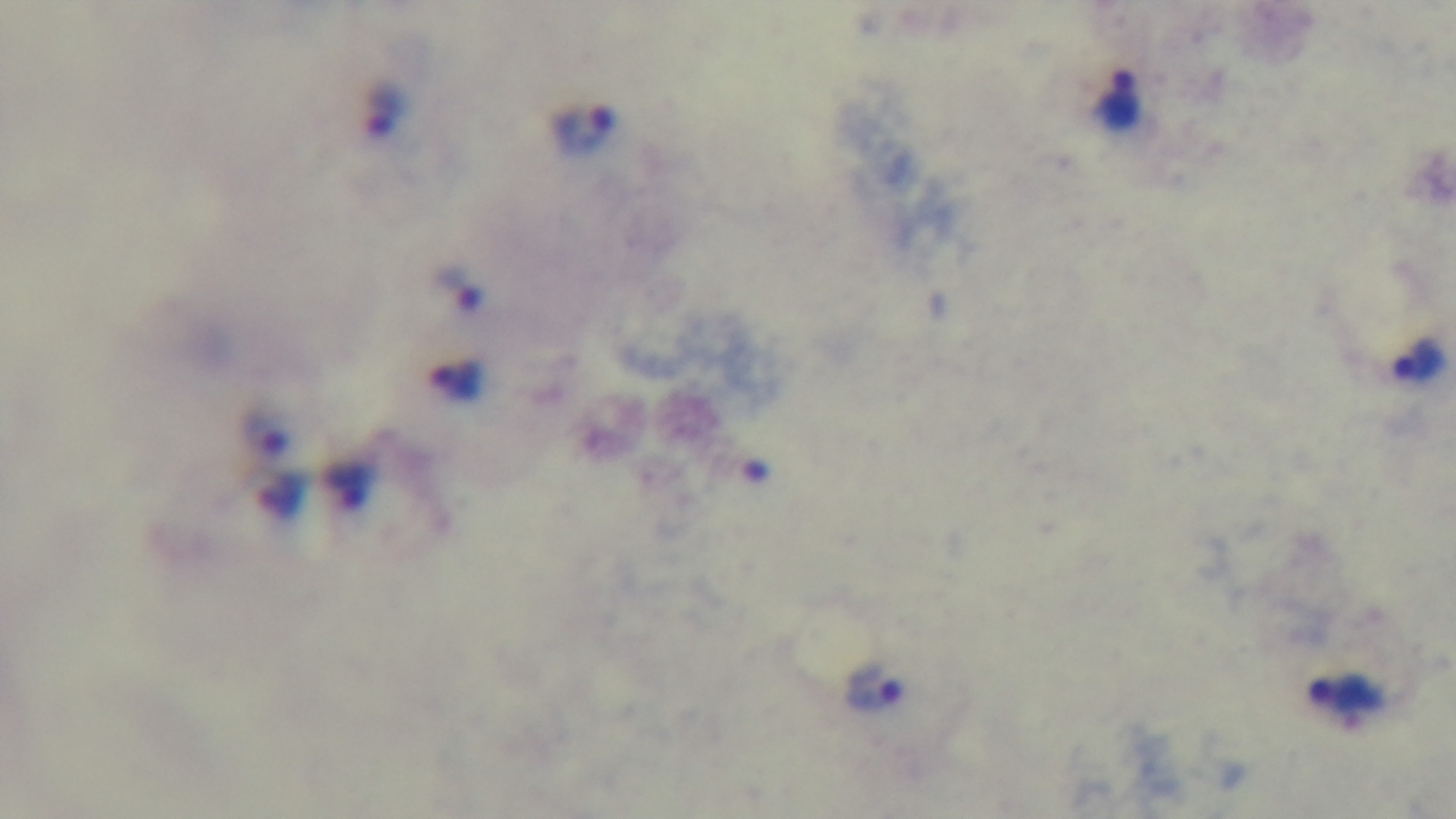

objective: 100x oil immersion
stain: Giemsa
capture: mounted 4K digital camera
preparation: thick
field_of_view: single
modality: light microscopy
malaria_status: infected